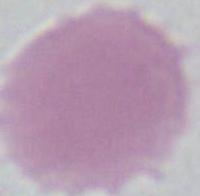

Summary:
  - Modality: photomicrograph
  - Magnification: 1000x
  - Identification: red blood cell